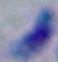

1000x magnification. Micrograph. Toxoplasma gondii is seen.